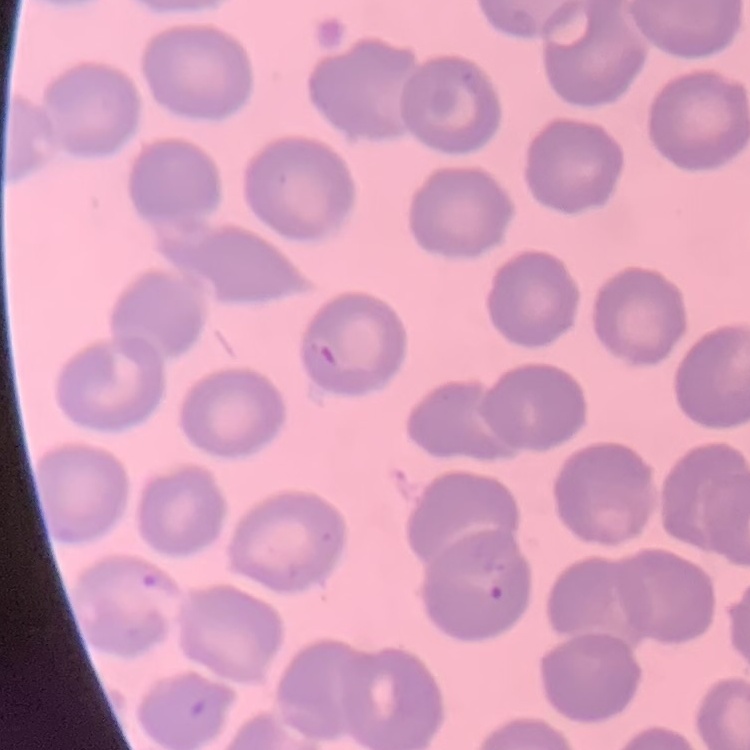
Summary:
  - Erythrocyte morphology: no rouleaux formation
  - Preparation: thin blood smear
  - Stain: Field's or Giemsa
  - Image type: square crop of a larger photomicrograph